Report the malaria status.
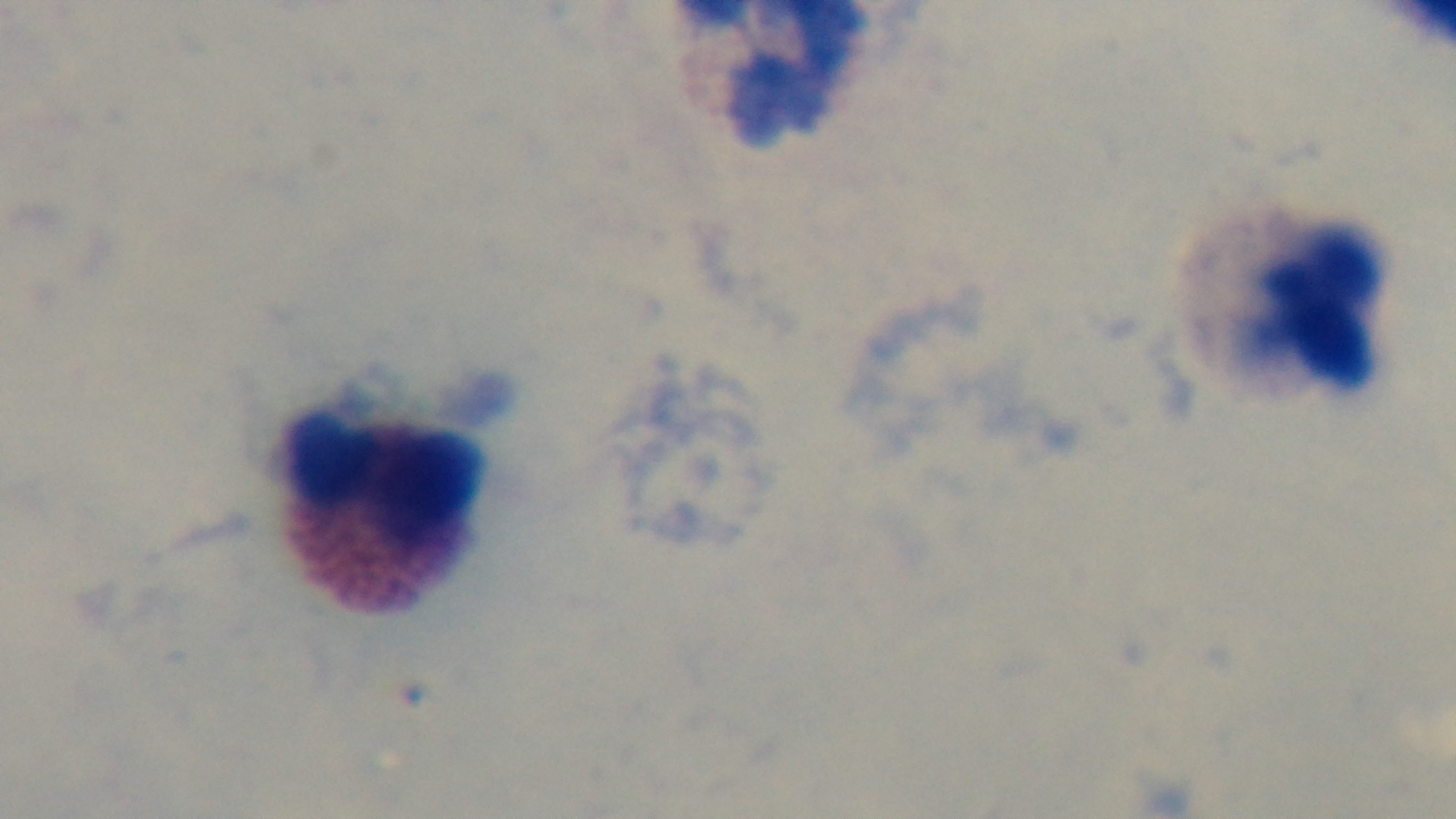
Uninfected.

Oil-immersion objective, 100x. Giemsa stain. Preparation: thick. Single field of view. Light microscopy. Captured with a mounted 4K digital camera.